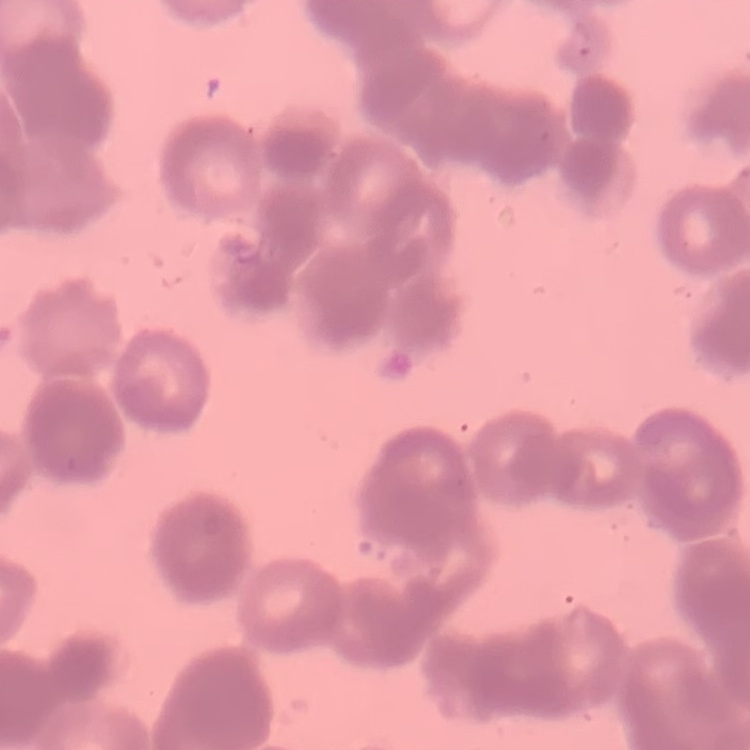
Summary:
  - Erythrocyte morphology: rouleaux formation
  - Preparation: thin blood film
  - Stain: Field's or Giemsa
  - Image type: square crop of a larger photomicrograph